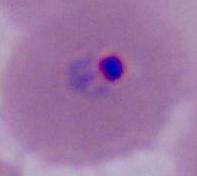
identification = Plasmodium
modality = photomicrograph
magnification = 400x or 1000x